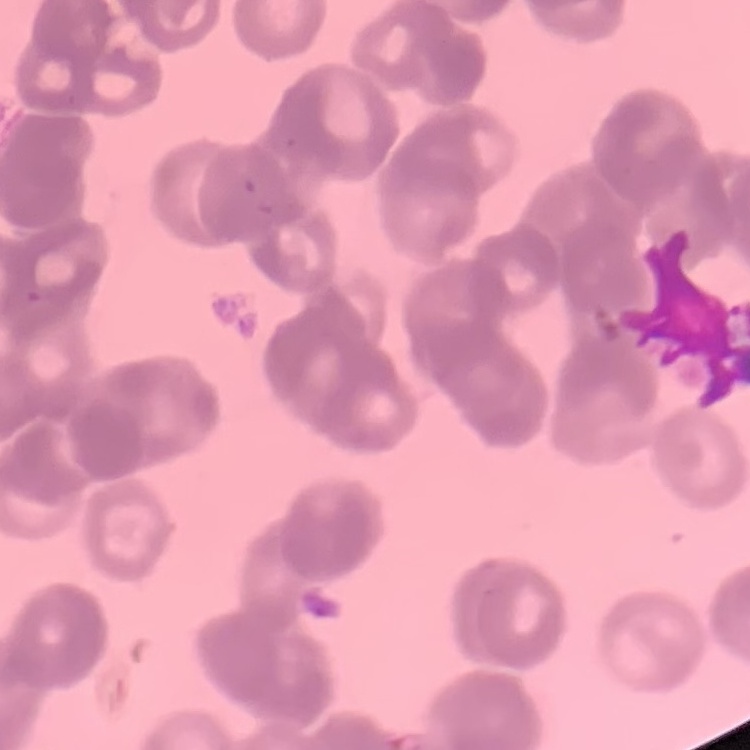

The erythrocytes show rouleaux formation. Field's or Giemsa stain. One tile cut from a larger photomicrograph. Thin peripheral smear.